Locate every Plasmodium parasite.
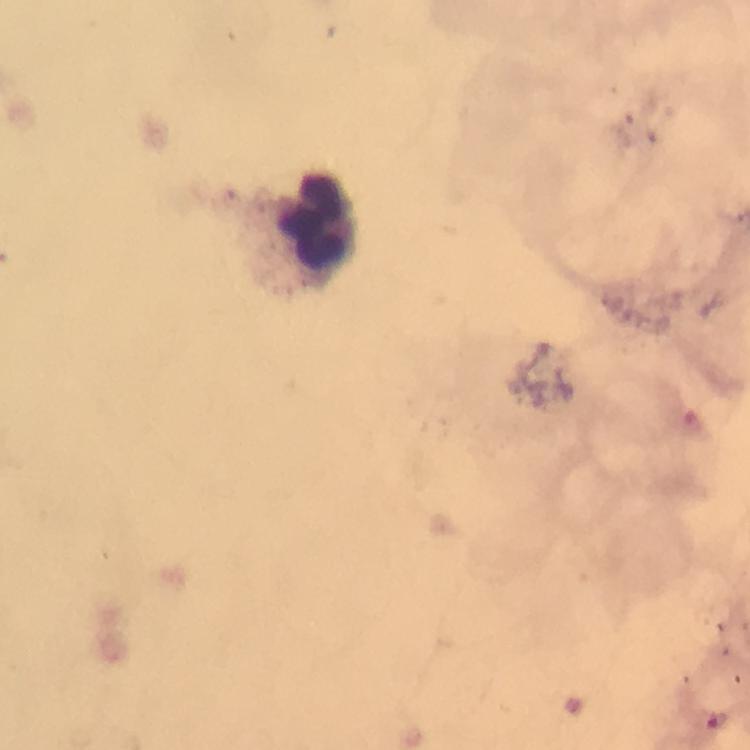
Approximate centers as (x, y) in pixels.
Plasmodium parasites: (721, 720).

Leukocyte locations: (314, 224). A crop from one field of view. Image is 750×750 pixels. Thick blood smear. At 100x magnification. From a diagnostic examination for malaria. Photographed with a smartphone mounted on the microscope. Immersion oil applied. Giemsa-stained preparation.